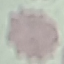

Summary:
  - Malaria status: uninfected
  - Preparation: thin blood film
  - Capture: smartphone camera at the microscope eyepiece
  - Image type: automatically extracted cell patch, resized to 64 × 64 pixels
  - Stain: Giemsa